State the preparation type.
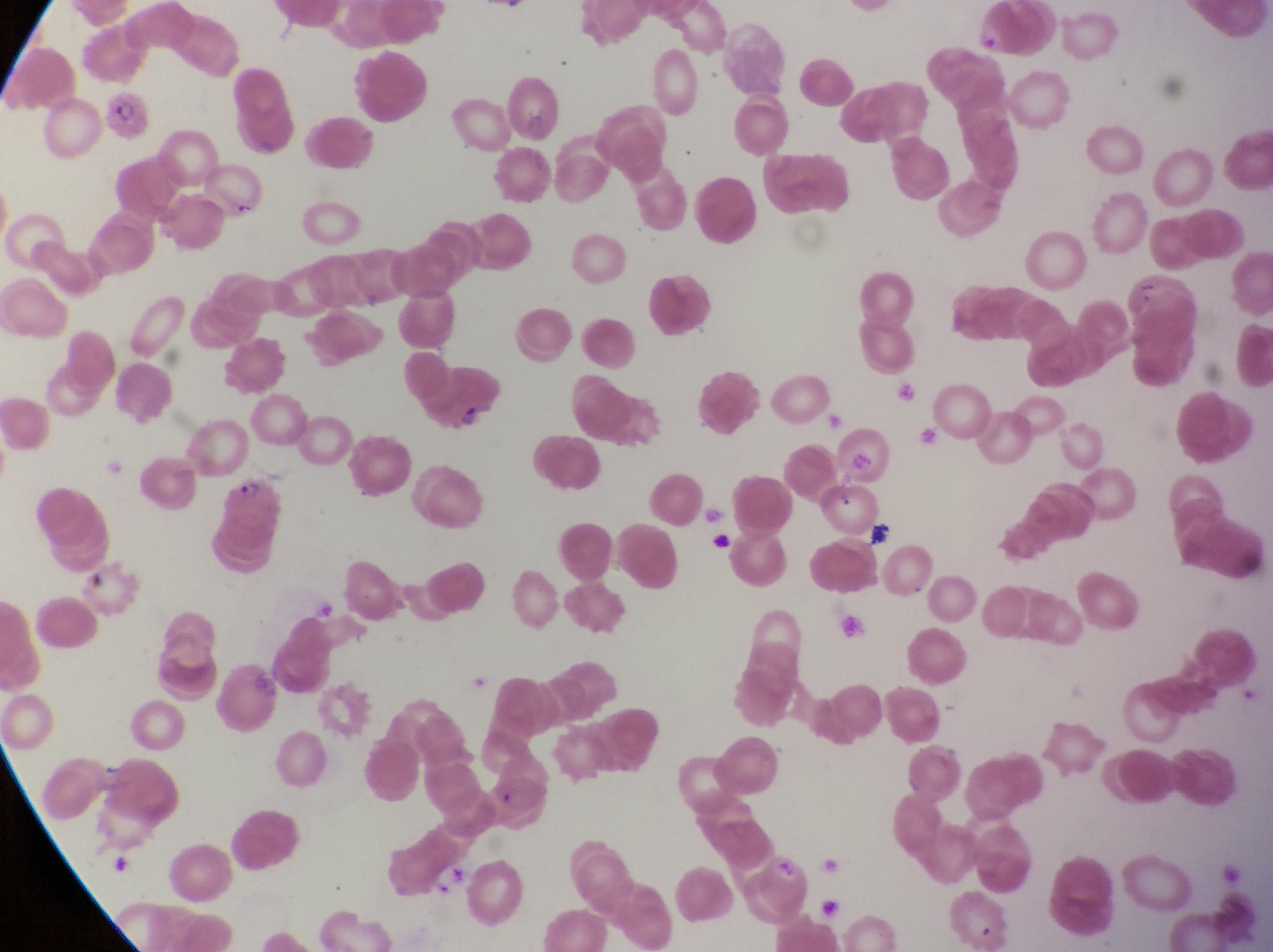
Thin blood film.

Approximate bounding boxes as (left, top, right, bottom) in pixels.
Summary:
  - Artifact (platelet-like body, stain precipitate, or debris) locations: (454, 402, 484, 434), (831, 487, 858, 517)
  - Parasitised red blood cell locations: (224, 475, 299, 537)
  - Country: Uganda
  - Image size: 1273×952 pixels
  - Field of view: single
  - Capture: smartphone photograph through the eyepiece of an Olympus CX-23 microscope
  - Magnification: 1000x